Assess this cell for malaria.
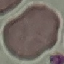
Uninfected.

Thin smear of blood. Photographed with a smartphone camera at the microscope eyepiece. Giemsa stain. Cell patch, automatically extracted from a larger field of view and resized to 64 × 64 pixels.